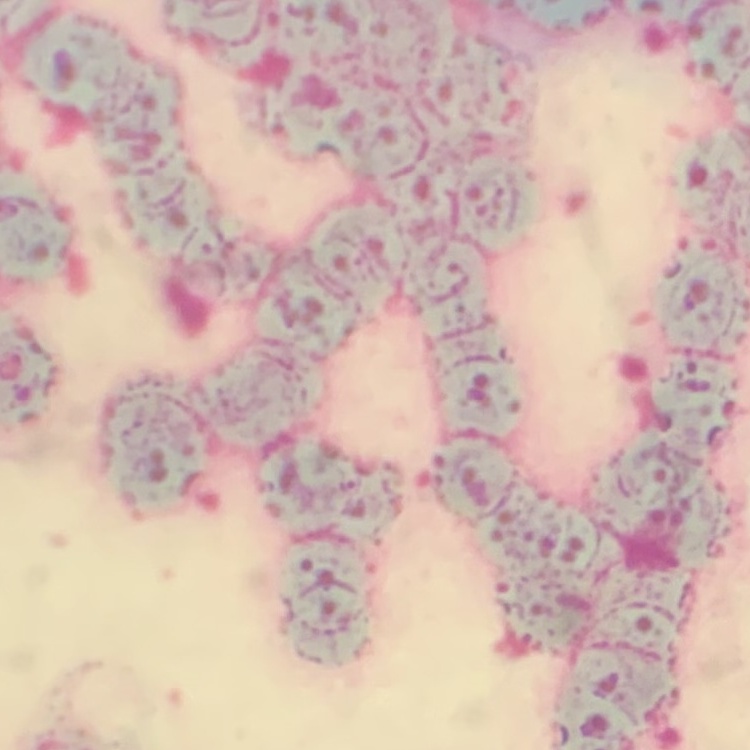

erythrocyte_morphology: rouleaux formation
stain: Field's or Giemsa
preparation: thin peripheral smear
image_type: square crop of a larger photomicrograph